Classify this cell by malaria status.
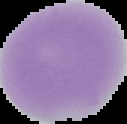

It is uninfected.

Segmented cell region on a black background. Image is 127×124 pixels. From a thin blood film.